Assess this cell for malaria.
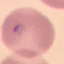
Parasitized.

Photographed with a smartphone camera at the microscope eyepiece. Thin smear of blood. Cell patch, automatically extracted from a larger field of view and resized to 64 × 64 pixels. Giemsa-stained preparation.